Describe the morphology of the erythrocytes.
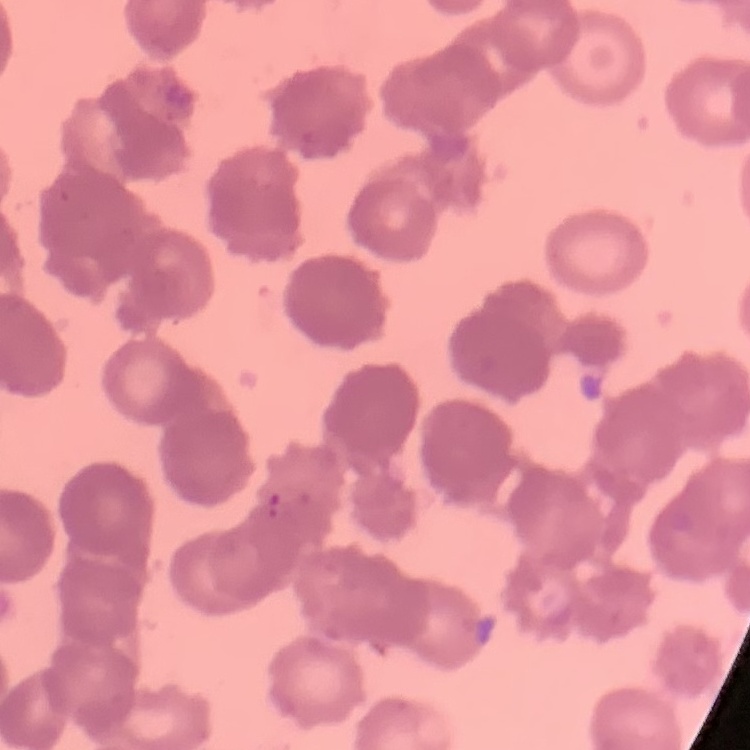

They show rouleaux formation.

One tile cut from a larger photomicrograph. Stained with either Field's or Giemsa. Thin blood smear.